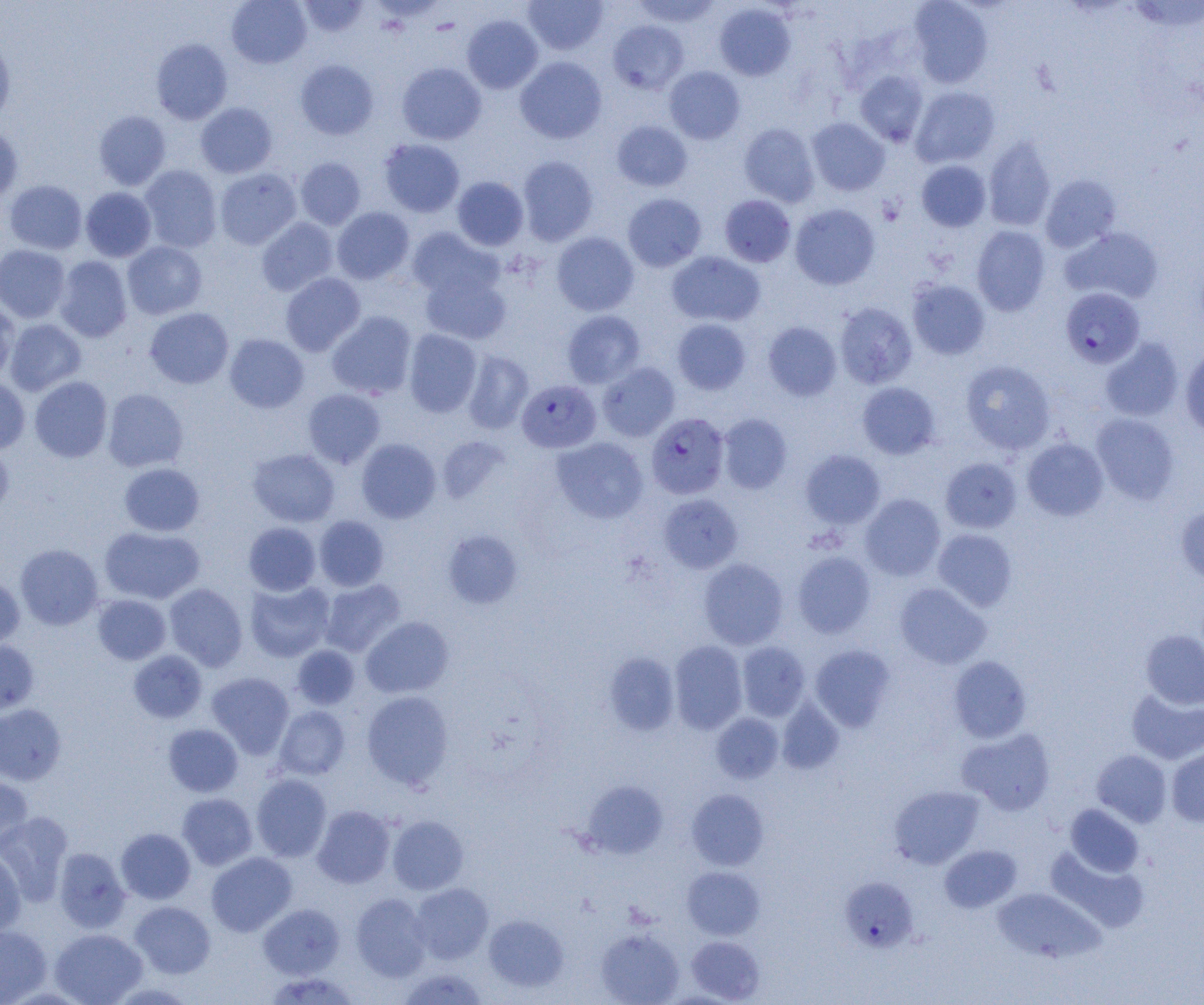
Approximate bounding boxes as [x1, y1, x2, y2] in pixels. Uninfected red blood cell locations: [227, 0, 311, 68], [297, 0, 369, 37], [523, 0, 608, 55], [631, 0, 722, 28], [908, 0, 993, 88], [1126, 1, 1204, 33], [714, 3, 796, 81], [462, 15, 543, 93], [608, 20, 689, 94], [0, 34, 15, 128], [151, 38, 233, 125], [515, 56, 607, 143], [295, 59, 378, 139], [396, 62, 486, 145], [664, 66, 745, 144], [854, 70, 928, 147], [911, 86, 1000, 168], [195, 102, 277, 178], [94, 110, 171, 190], [807, 118, 890, 195], [611, 120, 692, 192], [739, 122, 820, 207], [0, 127, 23, 204], [983, 136, 1056, 232], [379, 138, 465, 217], [295, 156, 366, 229], [517, 156, 598, 245], [916, 160, 991, 232], [139, 165, 222, 253], [214, 168, 301, 249], [1040, 174, 1122, 253], [452, 176, 529, 251], [4, 180, 87, 254], [80, 187, 156, 262], [623, 194, 706, 272], [719, 195, 796, 267], [790, 203, 880, 290], [332, 207, 414, 284], [256, 217, 338, 295], [971, 226, 1050, 315], [407, 227, 504, 301], [1060, 227, 1164, 305], [551, 231, 639, 316], [122, 241, 207, 320], [0, 244, 70, 323], [667, 251, 765, 327], [54, 256, 133, 342], [419, 269, 512, 345], [280, 272, 365, 356], [907, 279, 990, 360], [834, 302, 917, 389], [0, 303, 17, 384], [145, 307, 234, 389], [562, 310, 645, 388], [326, 311, 417, 399], [672, 318, 752, 395], [5, 319, 86, 395], [763, 321, 842, 400], [404, 330, 481, 417], [225, 333, 309, 413], [1099, 337, 1184, 422], [1180, 346, 1204, 437], [462, 349, 534, 434], [960, 359, 1056, 454], [597, 362, 680, 441], [0, 376, 30, 454], [29, 376, 112, 462], [857, 382, 941, 459], [103, 388, 188, 472], [303, 389, 385, 468], [1091, 413, 1179, 505], [717, 414, 792, 494], [438, 436, 510, 504], [552, 437, 649, 523], [356, 438, 441, 523], [1022, 438, 1108, 520], [0, 443, 14, 517], [248, 448, 340, 527], [800, 450, 886, 529], [940, 457, 1021, 533], [119, 463, 205, 536], [860, 493, 946, 581], [658, 494, 743, 573], [1176, 505, 1204, 585], [314, 515, 389, 591], [243, 522, 321, 596], [100, 526, 205, 604], [933, 528, 1017, 611], [442, 529, 524, 609], [16, 543, 104, 630], [792, 551, 876, 638], [698, 558, 788, 649], [0, 575, 24, 651], [319, 578, 406, 657], [244, 580, 335, 662], [164, 583, 247, 671], [894, 583, 991, 669], [93, 594, 171, 664], [361, 616, 454, 698], [1140, 630, 1204, 709], [669, 640, 748, 734], [0, 641, 39, 714], [736, 642, 809, 721], [292, 645, 360, 710], [809, 645, 896, 731], [129, 650, 207, 723], [603, 651, 679, 735], [948, 655, 1031, 743], [206, 672, 294, 759], [1127, 687, 1204, 765], [362, 691, 454, 790], [777, 699, 844, 774], [0, 703, 66, 785], [274, 705, 351, 780], [711, 712, 783, 783], [163, 723, 243, 797], [957, 727, 1056, 815], [1166, 745, 1204, 827], [1092, 749, 1171, 827], [251, 774, 331, 862], [0, 776, 34, 854], [581, 780, 668, 859], [889, 785, 984, 869], [686, 788, 769, 870], [177, 793, 257, 870], [1065, 804, 1144, 877], [312, 805, 395, 888], [0, 812, 73, 905], [387, 815, 469, 895], [115, 828, 196, 904], [939, 844, 1022, 913], [1045, 845, 1149, 932], [54, 847, 130, 933], [0, 848, 26, 937], [206, 852, 297, 936], [682, 866, 764, 939], [410, 883, 493, 963], [992, 888, 1104, 964], [351, 893, 431, 981], [130, 901, 215, 978], [259, 903, 344, 979], [484, 914, 568, 992], [0, 925, 51, 1004], [49, 928, 147, 1004], [595, 929, 684, 1005], [686, 936, 764, 1003], [398, 967, 488, 1004], [264, 973, 360, 1005]. Plasmodium falciparum-infected red blood cell locations: [1060, 287, 1145, 368], [521, 381, 605, 454], [646, 413, 729, 499], [842, 874, 918, 948]. Slide-level diagnosis: Plasmodium falciparum. Light microscopy. Single field of view. Image is 1204×1005 pixels. Thin blood smear. Captured at 1000x magnification.